Give the position of every leukocyte visible.
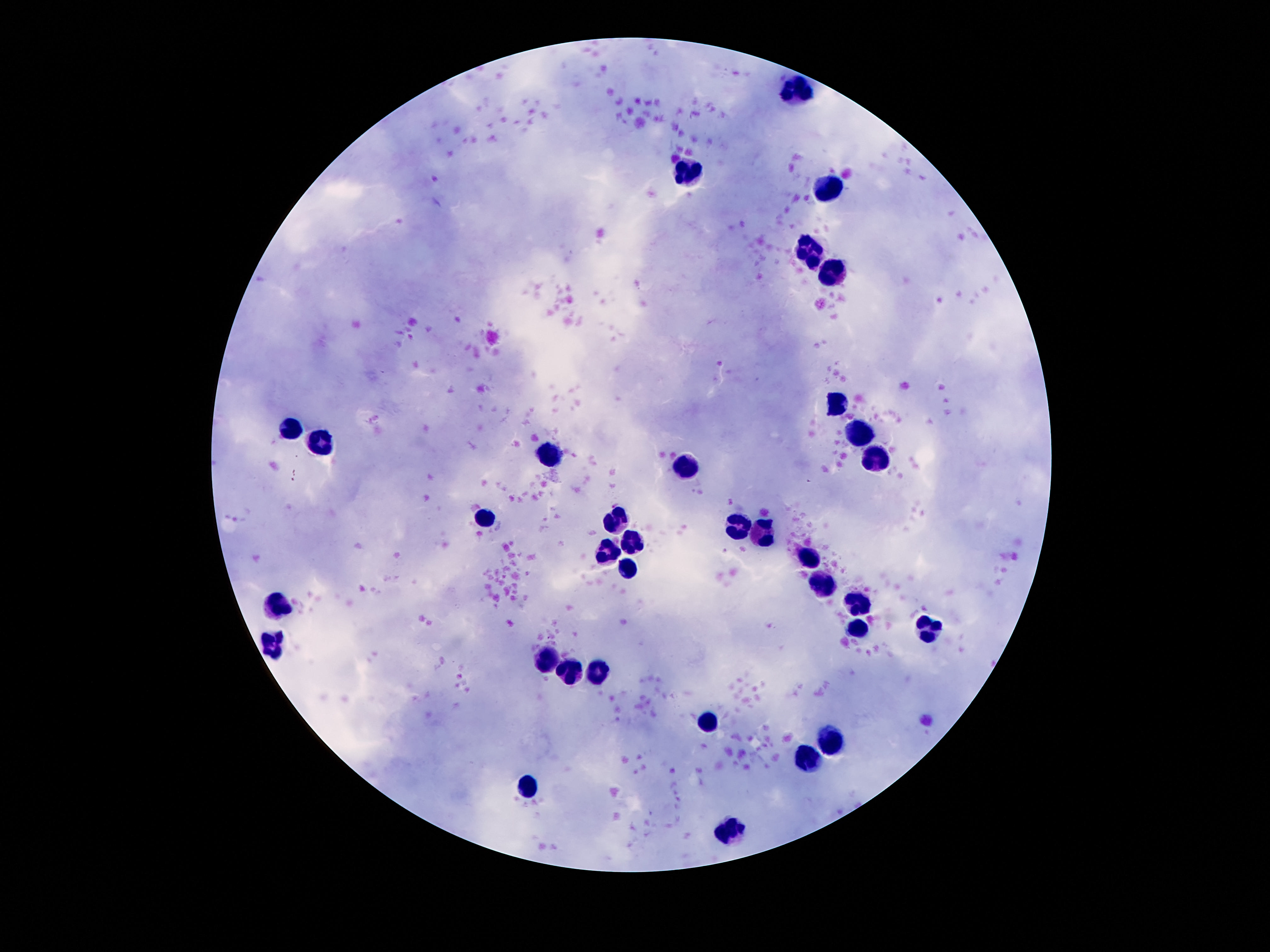
Approximate centers as [x, y] in pixels.
Leukocytes: [797, 90], [687, 175], [830, 189], [810, 253], [832, 271], [838, 406], [287, 431], [861, 437], [326, 439], [549, 457], [869, 463], [689, 468], [486, 517], [619, 522], [740, 527], [760, 533], [635, 543], [607, 554], [810, 561], [629, 570], [820, 587], [859, 603], [279, 605], [857, 630], [928, 630], [277, 643], [547, 660], [601, 668], [568, 671], [711, 720], [832, 742], [812, 761], [531, 785], [730, 832].

capture: smartphone camera through the microscope eyepiece
field_of_view: one from this slide
image_size: 1270×952 pixels
patient_malaria_status: uninfected
stain: Giemsa
preparation: thick peripheral-blood smear
magnification: 100x